Outline each blood parasite and name the species.
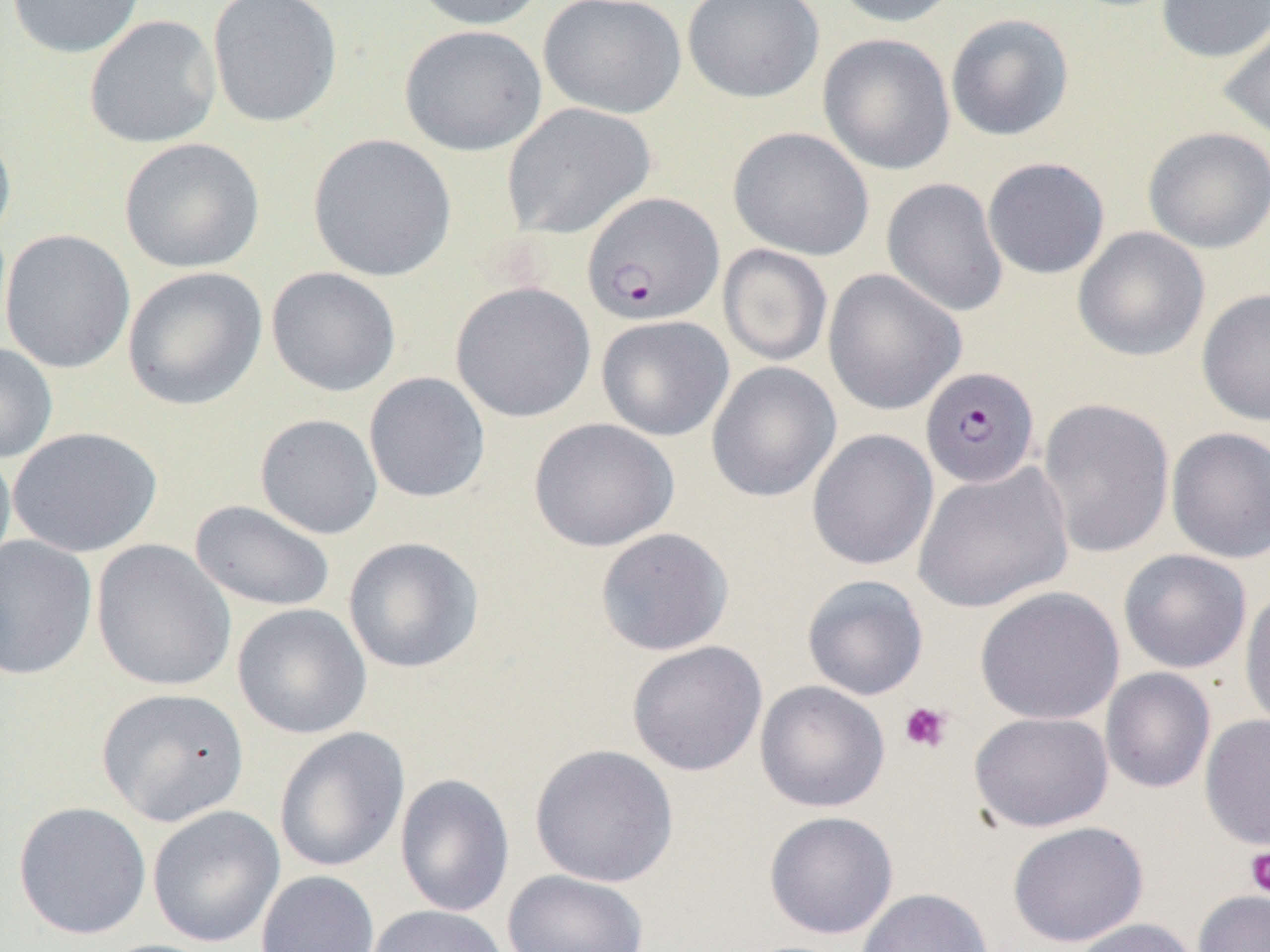

Approximate bounding boxes as (x1, y1, x2, y2) in pixels.
Plasmodium falciparum-infected red blood cells: (585, 193, 727, 328), (920, 366, 1040, 489).
No Plasmodium ovale, Plasmodium malariae, Plasmodium vivax, Babesia divergens, or Trypanosoma brucei observed.

Summary:
  - Platelet locations: (899, 701, 953, 753), (1244, 847, 1270, 897)
  - Uninfected red blood cell locations: (6, 0, 147, 59), (207, 0, 343, 127), (404, 0, 549, 31), (538, 0, 687, 119), (681, 0, 825, 104), (829, 0, 963, 28), (1156, 0, 1270, 63), (945, 13, 1074, 141), (84, 15, 222, 149), (1217, 16, 1270, 144), (399, 23, 547, 157), (817, 33, 956, 176), (501, 102, 656, 240), (0, 120, 17, 252), (728, 126, 875, 261), (1142, 126, 1270, 254), (307, 134, 457, 282), (118, 137, 265, 274), (982, 157, 1110, 279), (881, 177, 1009, 318), (1072, 226, 1210, 362), (1, 229, 136, 374), (718, 244, 832, 367), (122, 266, 268, 411), (266, 266, 402, 397), (822, 269, 967, 416), (450, 281, 596, 423), (1196, 287, 1270, 426), (596, 315, 734, 441), (0, 341, 58, 463), (706, 361, 841, 503), (363, 372, 491, 503), (1037, 398, 1175, 559), (254, 413, 383, 539), (528, 417, 679, 552), (8, 426, 162, 558), (1165, 426, 1270, 563), (806, 429, 939, 572), (0, 442, 16, 578), (912, 461, 1074, 614), (189, 499, 336, 613), (595, 527, 734, 656), (0, 535, 99, 681), (343, 536, 484, 673), (91, 539, 236, 691), (1118, 549, 1252, 673), (801, 574, 929, 701), (974, 586, 1125, 725), (1239, 587, 1270, 735), (232, 604, 371, 739), (626, 640, 768, 777), (1100, 668, 1216, 794), (754, 680, 891, 813), (96, 687, 249, 826), (968, 711, 1114, 832), (1199, 713, 1270, 851), (273, 726, 410, 873), (529, 743, 679, 888), (394, 773, 515, 918), (13, 801, 151, 939), (146, 804, 285, 948), (764, 811, 898, 939), (1006, 820, 1148, 947), (502, 869, 650, 952), (256, 870, 379, 952), (855, 887, 994, 951), (1192, 890, 1270, 952), (365, 904, 509, 952), (1069, 918, 1202, 952), (92, 939, 224, 952)
  - Slide-level diagnosis: Plasmodium falciparum
  - Field of view: one of a larger specimen
  - Image size: 1270×952 pixels
  - Magnification: 1000x
  - Preparation: thin blood film
  - Modality: light microscopy